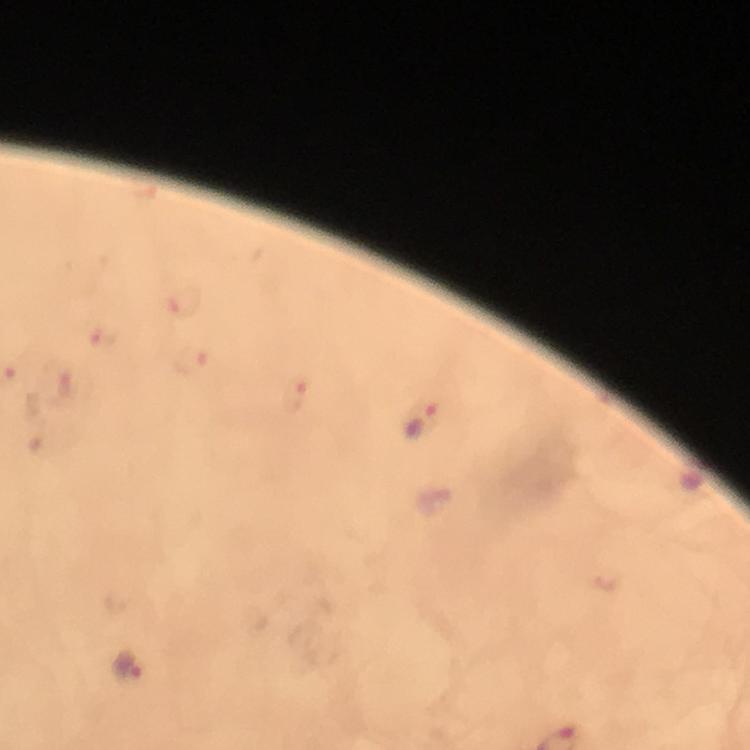

{
  "cropped_from": "a single field of view",
  "capture": "smartphone mounted on the microscope",
  "plasmodium_parasite_locations": "approximate object centers, in pixels from the top-left corner: (x=185, y=300), (x=105, y=338), (x=191, y=361), (x=295, y=394), (x=423, y=420), (x=128, y=665)",
  "image_size": "750×750 pixels",
  "preparation": "thick blood film",
  "immersion_oil": "applied",
  "magnification": "100x",
  "stain": "Giemsa",
  "context": "from a malaria diagnostic workup"
}